Give the extent of all Plasmodium vivax-infected red blood cells.
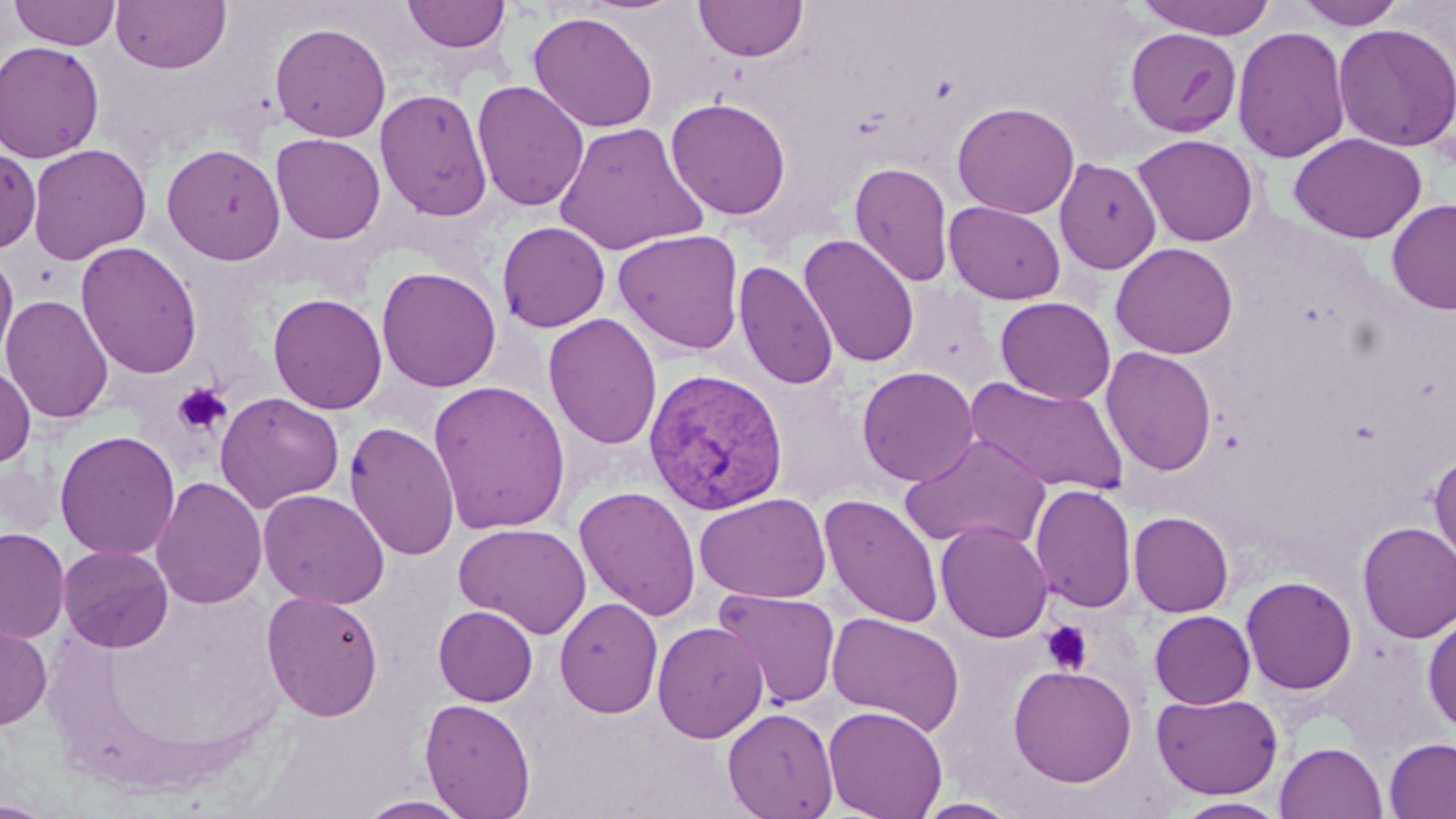

Approximate bounding boxes as [x1, y1, x2, y2] in pixels.
Plasmodium vivax-infected red blood cells: [643, 368, 789, 517].

Platelet locations: [172, 381, 232, 437], [1041, 620, 1093, 675]. Uninfected red blood cell locations: [8, 0, 121, 50], [111, 0, 230, 74], [402, 0, 512, 53], [694, 0, 808, 61], [1136, 0, 1277, 39], [1294, 0, 1406, 29], [527, 11, 659, 133], [270, 22, 391, 142], [1333, 22, 1456, 152], [1232, 26, 1351, 164], [1124, 27, 1242, 137], [0, 41, 105, 163], [472, 81, 590, 212], [374, 87, 493, 222], [665, 97, 791, 220], [952, 101, 1080, 219], [554, 121, 709, 256], [1290, 132, 1427, 244], [271, 133, 386, 245], [1132, 134, 1259, 247], [28, 143, 151, 264], [161, 143, 286, 265], [0, 147, 41, 254], [1055, 157, 1161, 274], [850, 161, 954, 288], [1387, 198, 1456, 315], [944, 200, 1067, 304], [497, 221, 611, 332], [613, 228, 745, 355], [799, 234, 920, 368], [76, 241, 202, 379], [1111, 242, 1238, 359], [0, 250, 19, 373], [733, 260, 838, 390], [376, 266, 502, 392], [268, 293, 387, 414], [1, 294, 114, 424], [995, 297, 1115, 405], [543, 313, 663, 450], [1100, 346, 1218, 476], [0, 365, 36, 468], [857, 366, 979, 487], [762, 370, 880, 509], [966, 376, 1130, 497], [428, 380, 570, 534], [215, 392, 345, 512], [344, 421, 461, 562], [54, 430, 180, 561], [901, 434, 1051, 552], [1429, 450, 1456, 568], [151, 476, 267, 609], [1030, 484, 1136, 614], [574, 485, 702, 621], [258, 489, 391, 610], [695, 493, 831, 604], [819, 494, 943, 629], [1129, 511, 1234, 617], [1357, 521, 1456, 643], [454, 522, 592, 639], [936, 522, 1053, 643], [0, 527, 70, 643], [58, 544, 173, 652], [1240, 575, 1358, 695], [713, 587, 841, 710], [261, 591, 384, 722], [555, 597, 663, 718], [431, 605, 663, 710], [434, 605, 538, 706], [1150, 610, 1255, 709], [827, 612, 965, 736], [1423, 614, 1456, 733], [0, 617, 53, 732], [652, 621, 768, 743], [1008, 664, 1137, 787], [1152, 693, 1283, 800], [420, 698, 536, 819], [823, 704, 948, 819], [723, 707, 838, 819], [1384, 738, 1456, 819], [1275, 742, 1387, 819], [354, 796, 476, 818], [1173, 797, 1289, 818], [912, 798, 1024, 818]. Slide-level diagnosis: Plasmodium vivax. Light microscopy. Single field of view. Captured at 1000x magnification. May-Grünwald-Giemsa-stained preparation. Thin blood film. Image is 1456×819 pixels.